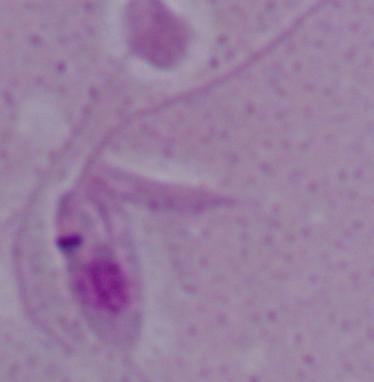
magnification = 1000x
modality = micrograph
identification = Leishmania